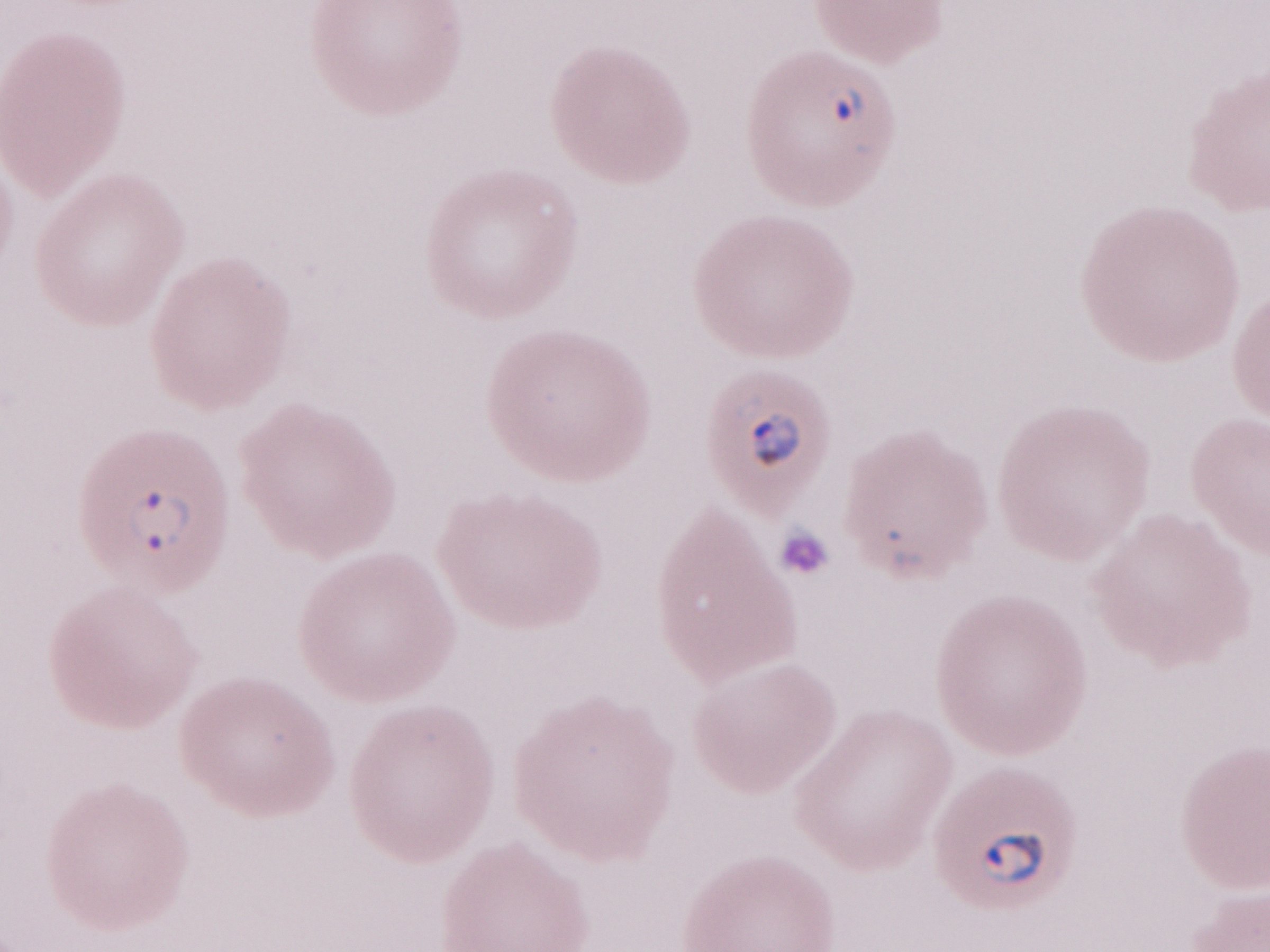 Magnification: 1,000x. May-Grünwald-Giemsa-stained preparation. Image is 1270×952 pixels. Olympus BX43 microscope, Olympus DP73 camera. Thin blood smear. One field of this slide. Patient-level malaria diagnosis: positive.